Classify this cell by malaria status.
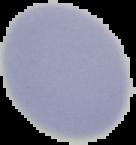
It is uninfected.

Summary:
  - Image type: segmented cell region with the area outside set to black
  - Preparation: thin blood smear
  - Image size: 136×145 pixels